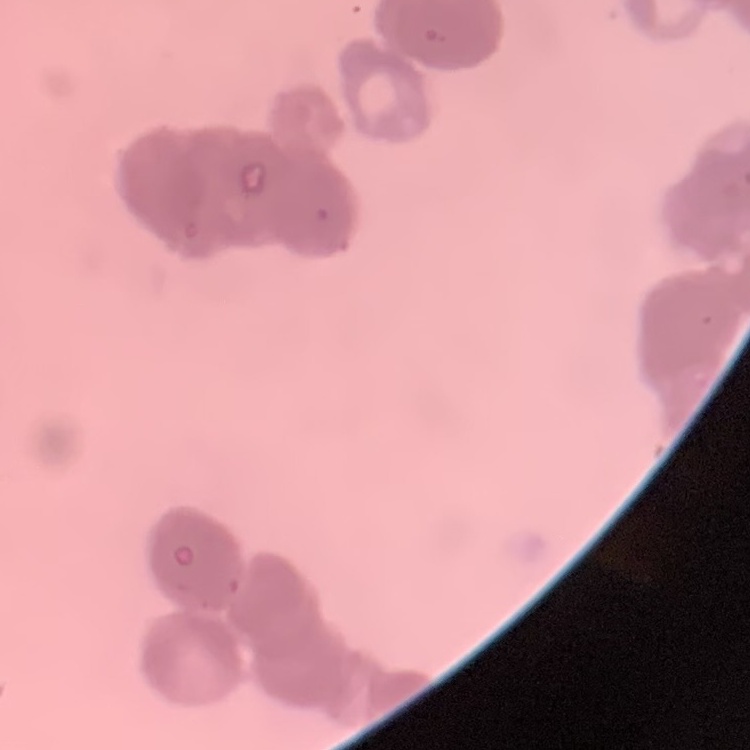

The erythrocytes exhibit rouleaux formation. Field's or Giemsa stain. Thin peripheral smear. Square crop of a larger photomicrograph.